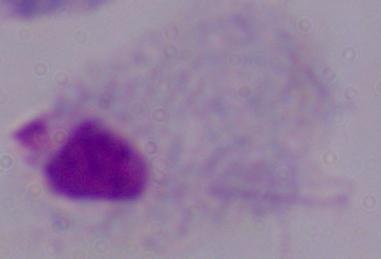

magnification: 1000x
modality: micrograph
identification: trichomonad